Name the blood parasite species.
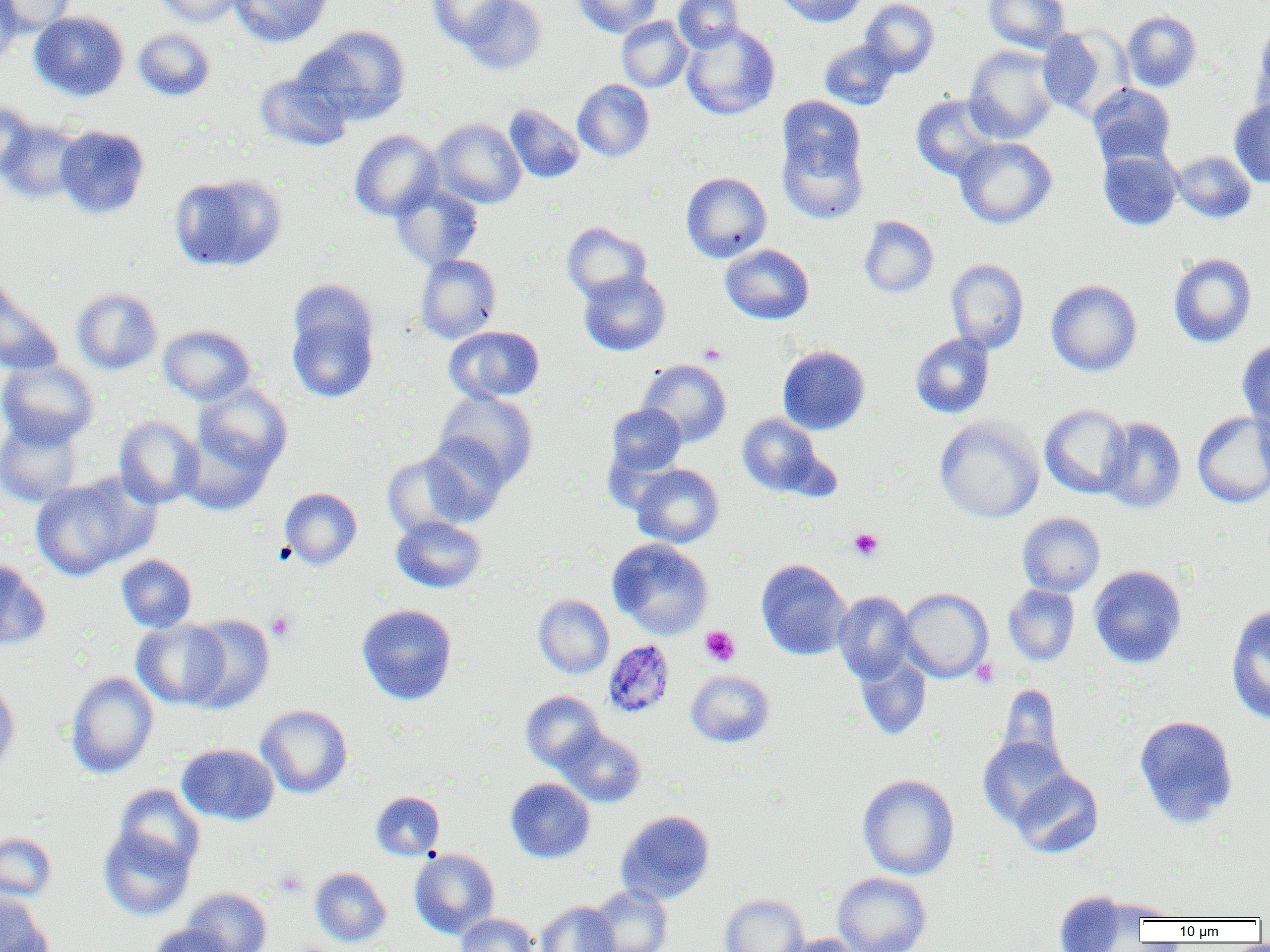

Plasmodium malariae.

Summary:
  - Coordinate format: approximate bounding boxes as named x1/y1/x2/y2 corners in pixels
  - Uninfected red blood cell locations: (x1=0, y1=0, x2=23, y2=66), (x1=1, y1=0, x2=76, y2=36), (x1=153, y1=0, x2=245, y2=26), (x1=229, y1=0, x2=332, y2=47), (x1=428, y1=0, x2=514, y2=47), (x1=457, y1=0, x2=546, y2=75), (x1=574, y1=0, x2=662, y2=37), (x1=673, y1=0, x2=744, y2=52), (x1=774, y1=0, x2=866, y2=27), (x1=860, y1=0, x2=939, y2=77), (x1=984, y1=0, x2=1070, y2=53), (x1=1121, y1=10, x2=1202, y2=92), (x1=29, y1=11, x2=129, y2=101), (x1=617, y1=16, x2=692, y2=92), (x1=1250, y1=21, x2=1270, y2=120), (x1=680, y1=23, x2=780, y2=120), (x1=301, y1=25, x2=411, y2=125), (x1=1037, y1=26, x2=1129, y2=119), (x1=133, y1=28, x2=215, y2=101), (x1=819, y1=39, x2=899, y2=110), (x1=964, y1=45, x2=1059, y2=143), (x1=254, y1=71, x2=353, y2=152), (x1=573, y1=79, x2=654, y2=161), (x1=1088, y1=84, x2=1176, y2=168), (x1=911, y1=94, x2=1004, y2=181), (x1=778, y1=96, x2=866, y2=183), (x1=1229, y1=100, x2=1270, y2=187), (x1=0, y1=102, x2=39, y2=178), (x1=504, y1=104, x2=584, y2=183), (x1=431, y1=119, x2=526, y2=208), (x1=0, y1=120, x2=87, y2=204), (x1=54, y1=125, x2=149, y2=219), (x1=349, y1=129, x2=443, y2=221), (x1=778, y1=132, x2=867, y2=224), (x1=955, y1=137, x2=1057, y2=229), (x1=1098, y1=148, x2=1182, y2=231), (x1=1172, y1=150, x2=1255, y2=223), (x1=681, y1=172, x2=771, y2=262), (x1=169, y1=173, x2=286, y2=272), (x1=391, y1=182, x2=483, y2=270), (x1=858, y1=216, x2=938, y2=297), (x1=562, y1=222, x2=651, y2=302), (x1=720, y1=244, x2=813, y2=324), (x1=1168, y1=253, x2=1257, y2=348), (x1=416, y1=254, x2=501, y2=343), (x1=946, y1=259, x2=1029, y2=353), (x1=579, y1=270, x2=670, y2=356), (x1=0, y1=274, x2=64, y2=376), (x1=288, y1=278, x2=378, y2=361), (x1=1046, y1=279, x2=1142, y2=376), (x1=72, y1=288, x2=162, y2=374), (x1=287, y1=306, x2=378, y2=403), (x1=159, y1=325, x2=255, y2=405), (x1=444, y1=325, x2=545, y2=404), (x1=910, y1=333, x2=994, y2=418), (x1=1237, y1=339, x2=1270, y2=430), (x1=778, y1=345, x2=870, y2=435), (x1=0, y1=359, x2=99, y2=448), (x1=637, y1=359, x2=731, y2=447), (x1=193, y1=383, x2=292, y2=477), (x1=434, y1=391, x2=539, y2=487), (x1=606, y1=403, x2=686, y2=477), (x1=1040, y1=404, x2=1133, y2=498), (x1=1192, y1=412, x2=1270, y2=508), (x1=738, y1=413, x2=825, y2=496), (x1=0, y1=415, x2=84, y2=507), (x1=114, y1=416, x2=204, y2=508), (x1=934, y1=417, x2=1044, y2=522), (x1=1099, y1=417, x2=1186, y2=513), (x1=178, y1=429, x2=274, y2=515), (x1=421, y1=435, x2=510, y2=526), (x1=382, y1=452, x2=474, y2=537), (x1=631, y1=464, x2=724, y2=548), (x1=30, y1=475, x2=154, y2=580), (x1=280, y1=487, x2=362, y2=569), (x1=1017, y1=512, x2=1105, y2=596), (x1=391, y1=516, x2=486, y2=593), (x1=608, y1=538, x2=713, y2=639), (x1=116, y1=554, x2=197, y2=632), (x1=0, y1=559, x2=51, y2=651), (x1=756, y1=559, x2=852, y2=660), (x1=1089, y1=565, x2=1187, y2=668), (x1=1003, y1=585, x2=1079, y2=666), (x1=899, y1=588, x2=993, y2=682), (x1=833, y1=591, x2=916, y2=683), (x1=533, y1=595, x2=614, y2=678), (x1=1225, y1=603, x2=1270, y2=725), (x1=357, y1=604, x2=457, y2=704), (x1=181, y1=615, x2=275, y2=713), (x1=131, y1=618, x2=231, y2=709), (x1=854, y1=651, x2=932, y2=740), (x1=686, y1=670, x2=775, y2=747), (x1=66, y1=671, x2=158, y2=779), (x1=0, y1=678, x2=19, y2=777), (x1=996, y1=684, x2=1065, y2=768), (x1=521, y1=691, x2=604, y2=772), (x1=255, y1=704, x2=353, y2=798), (x1=1134, y1=715, x2=1238, y2=829), (x1=556, y1=727, x2=646, y2=808), (x1=979, y1=736, x2=1073, y2=827), (x1=177, y1=743, x2=279, y2=825), (x1=1010, y1=769, x2=1103, y2=858), (x1=858, y1=774, x2=959, y2=880), (x1=506, y1=778, x2=595, y2=863), (x1=113, y1=785, x2=204, y2=873), (x1=371, y1=791, x2=444, y2=860), (x1=616, y1=810, x2=715, y2=904), (x1=98, y1=826, x2=195, y2=920), (x1=0, y1=833, x2=57, y2=901), (x1=409, y1=849, x2=499, y2=938), (x1=310, y1=867, x2=391, y2=947), (x1=832, y1=872, x2=931, y2=952), (x1=588, y1=885, x2=672, y2=951), (x1=182, y1=888, x2=271, y2=952), (x1=1054, y1=891, x2=1137, y2=951), (x1=0, y1=892, x2=53, y2=952), (x1=720, y1=894, x2=809, y2=952), (x1=535, y1=900, x2=619, y2=952), (x1=456, y1=913, x2=538, y2=952), (x1=148, y1=923, x2=236, y2=952), (x1=778, y1=934, x2=860, y2=952)
  - Platelet locations: (x1=699, y1=342, x2=726, y2=365), (x1=849, y1=529, x2=883, y2=560), (x1=266, y1=612, x2=295, y2=642), (x1=701, y1=626, x2=740, y2=666), (x1=971, y1=659, x2=998, y2=687), (x1=274, y1=870, x2=307, y2=897)
  - Plasmodium malariae-infected red blood cell locations: (x1=603, y1=639, x2=675, y2=717)
  - Magnification: 1000x
  - Field of view: one of a larger specimen
  - Image size: 1270×952 pixels
  - Modality: optical microscopy
  - Preparation: thin blood film